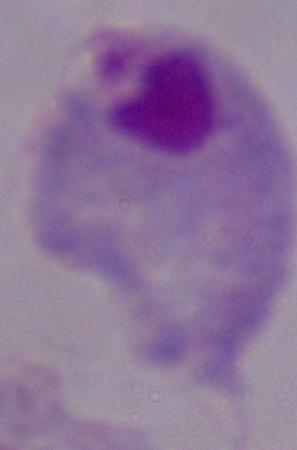

{
  "magnification": "1000x",
  "identification": "trichomonad",
  "modality": "photomicrograph"
}